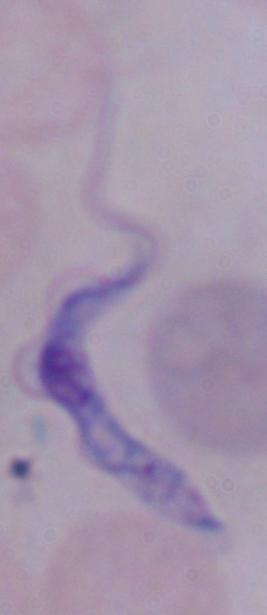

Summary:
  - Identification: trypanosome
  - Modality: photomicrograph
  - Magnification: 1000x